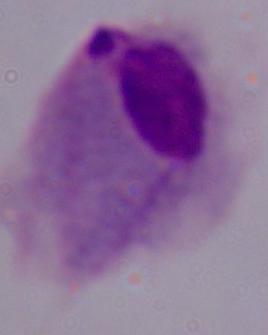 Micrograph. A trichomonad is shown. Captured at 1000x magnification.